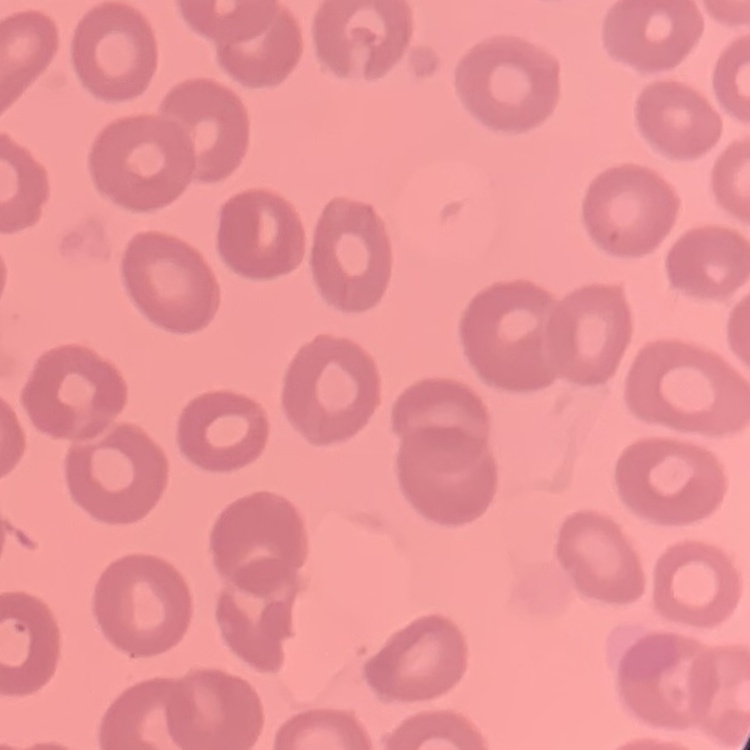

red_blood_cell_morphology: no rouleaux formation
stain: Field's or Giemsa
image_type: square crop of a larger photomicrograph
preparation: thin peripheral smear